Evaluate for malaria.
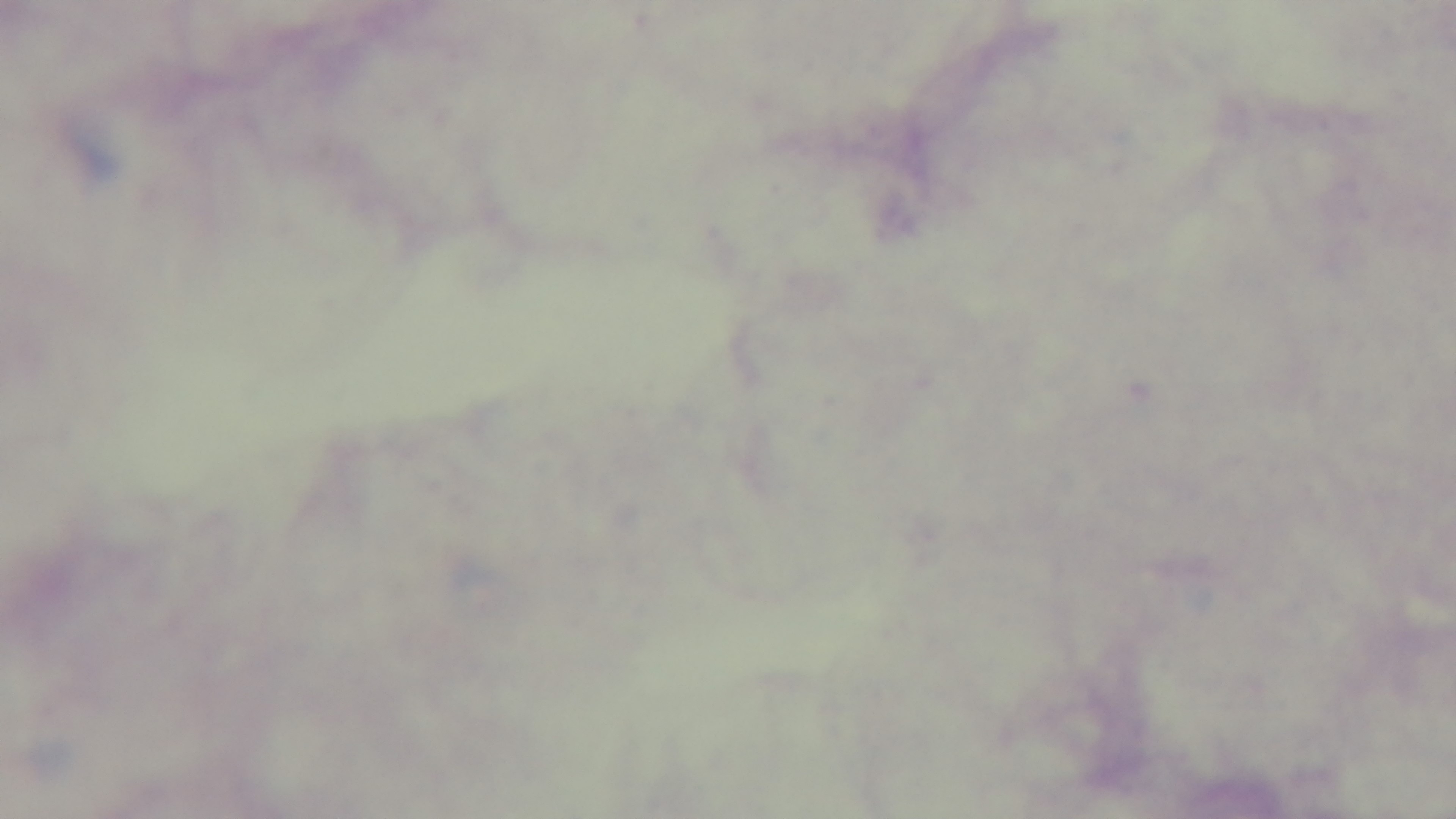
Uninfected.

Summary:
  - Stain: Giemsa
  - Objective: 100x oil immersion
  - Capture: mounted 4K digital camera
  - Preparation: thick
  - Field of view: one from the slide
  - Modality: light microscopy